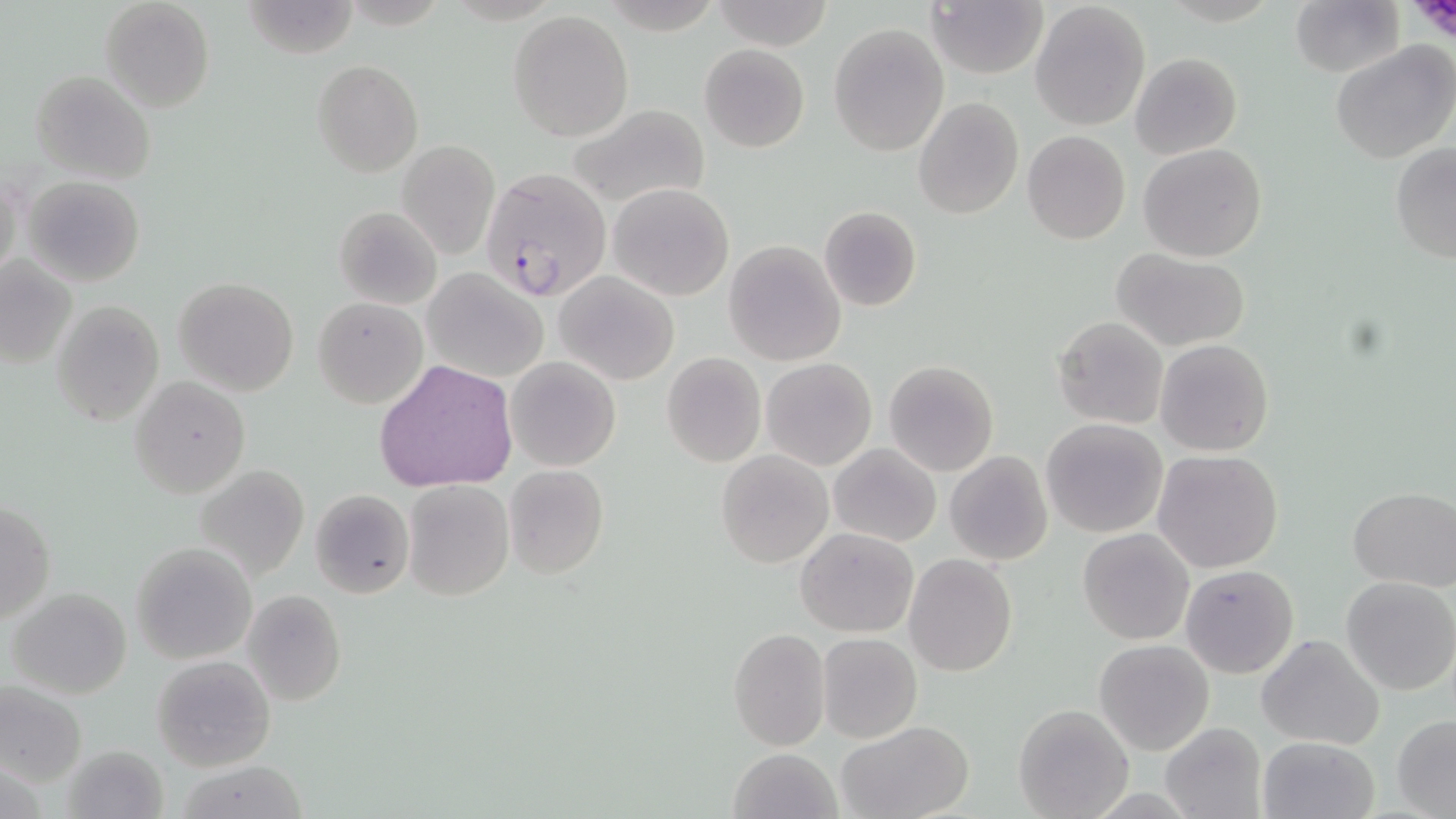

Summary:
  - Coordinate format: approximate bounding boxes as (x1, y1, x2, y2) in pixels
  - Platelet locations: (1403, 0, 1456, 40)
  - Uninfected red blood cell locations: (98, 0, 214, 113), (709, 0, 836, 51), (1290, 0, 1405, 76), (240, 1, 363, 58), (927, 1, 1048, 78), (1029, 2, 1152, 131), (508, 10, 633, 141), (828, 23, 948, 156), (1330, 40, 1456, 166), (699, 43, 809, 152), (1130, 52, 1243, 160), (312, 59, 424, 179), (31, 71, 154, 185), (913, 97, 1023, 219), (565, 104, 712, 212), (1023, 131, 1131, 245), (397, 140, 499, 259), (1390, 142, 1456, 265), (1139, 143, 1267, 262), (1, 170, 24, 285), (24, 176, 146, 287), (608, 181, 733, 301), (335, 205, 441, 308), (817, 206, 922, 313), (725, 240, 846, 365), (1112, 248, 1251, 350), (1, 256, 77, 370), (423, 267, 548, 383), (555, 270, 679, 386), (173, 277, 298, 395), (313, 296, 428, 409), (50, 300, 165, 427), (1053, 316, 1167, 429), (1155, 339, 1274, 456), (661, 352, 766, 467), (505, 357, 620, 471), (761, 357, 877, 469), (374, 360, 518, 492), (884, 360, 999, 475), (131, 377, 250, 497), (1041, 419, 1166, 537), (828, 443, 940, 546), (715, 449, 833, 567), (1155, 450, 1282, 573), (944, 451, 1053, 566), (194, 463, 310, 583), (503, 465, 609, 581), (405, 479, 513, 601), (308, 487, 415, 599), (1348, 487, 1455, 590), (1, 498, 54, 626), (796, 526, 919, 637), (1078, 529, 1194, 644), (130, 542, 257, 665), (903, 554, 1017, 676), (1180, 564, 1299, 679), (1340, 576, 1456, 695), (7, 586, 133, 698), (244, 590, 347, 705), (726, 627, 830, 751), (816, 632, 922, 744), (1255, 633, 1385, 749), (1095, 638, 1215, 756), (151, 655, 275, 771), (1, 681, 87, 788), (1014, 703, 1136, 819), (1392, 715, 1456, 817), (835, 721, 975, 819), (1160, 723, 1266, 818), (1257, 735, 1379, 819), (60, 744, 171, 819), (728, 747, 842, 819), (175, 760, 313, 818)
  - Plasmodium falciparum-infected red blood cell locations: (481, 168, 612, 304)
  - Slide-level diagnosis: Plasmodium falciparum
  - Field of view: one of a larger specimen
  - Modality: light microscopy
  - Magnification: 1000x
  - Stain: May-Grünwald-Giemsa
  - Preparation: thin blood film
  - Image size: 1456×819 pixels